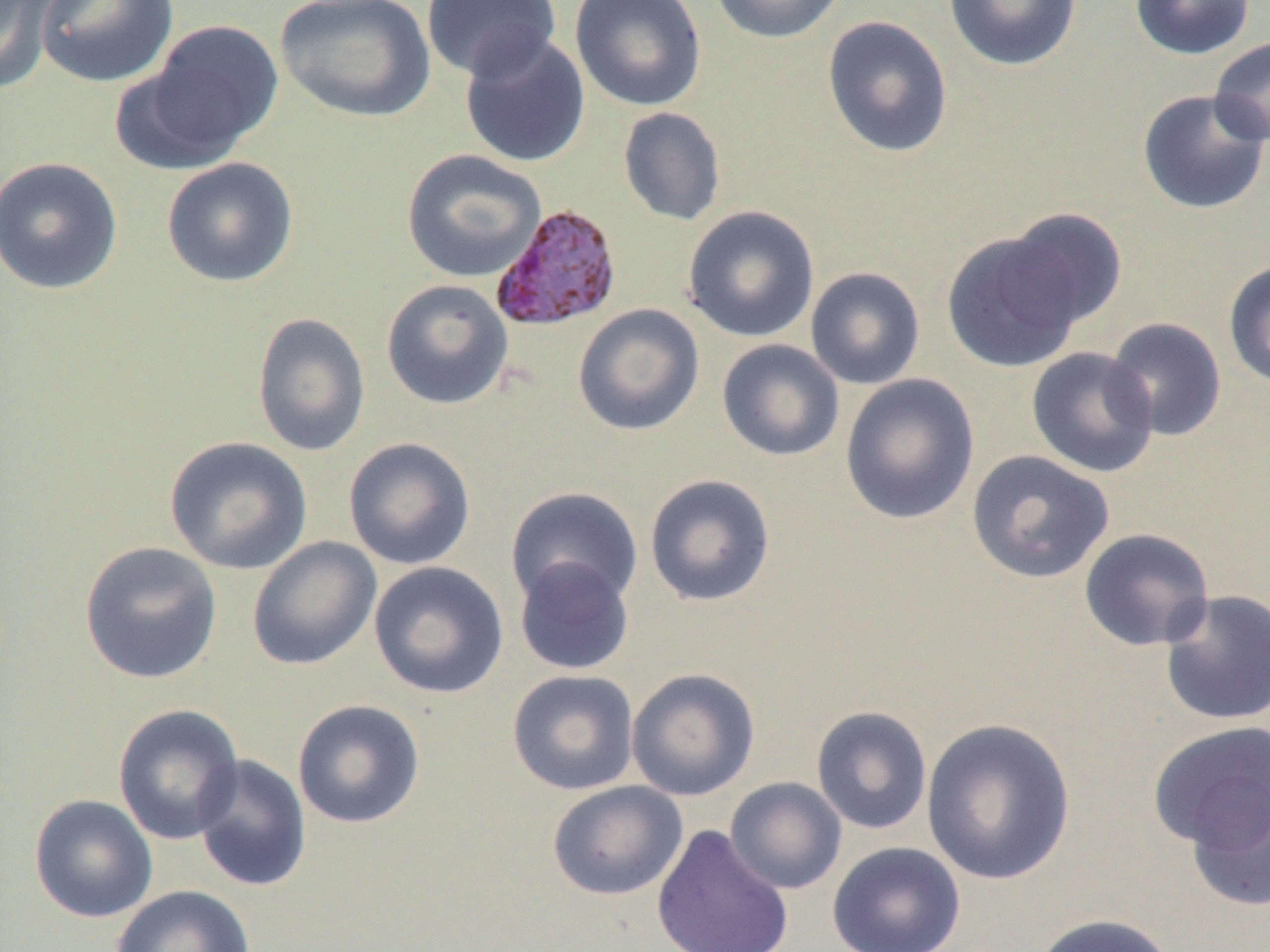

slide_level_diagnosis: Plasmodium vivax
field_of_view: one of a larger specimen
image_size: 1270×952 pixels
plasmodium_vivax_infected_red_blood_cell_locations: 'approximate bounding boxes as (x1, y1, x2, y2) in pixels: (490, 203, 622, 331)'
preparation: thin blood smear
magnification: 1000x
modality: light microscopy
uninfected_red_blood_cell_locations: 'approximate bounding boxes as (x1, y1, x2, y2) in pixels: (1, 0, 60, 94), (36, 0, 178, 88), (275, 0, 436, 123), (421, 0, 561, 82), (570, 0, 707, 112), (710, 0, 846, 44), (943, 0, 1083, 72), (1130, 0, 1255, 60), (821, 15, 954, 158), (140, 20, 284, 161), (459, 32, 591, 168), (1209, 36, 1270, 147), (1136, 89, 1270, 215), (618, 107, 726, 226), (401, 149, 547, 283), (0, 156, 123, 295), (161, 157, 298, 287), (682, 205, 820, 343), (1003, 208, 1128, 329), (941, 230, 1086, 373), (1223, 260, 1270, 389), (805, 266, 926, 390), (381, 279, 514, 410), (573, 303, 705, 436), (252, 311, 371, 457), (1104, 317, 1227, 441), (716, 338, 845, 461), (1026, 346, 1160, 479), (839, 373, 979, 525), (164, 436, 313, 575), (342, 436, 476, 570), (966, 449, 1115, 584), (644, 474, 776, 607), (505, 486, 644, 611), (1079, 527, 1215, 652), (247, 536, 382, 670), (79, 541, 223, 685), (514, 557, 635, 676), (368, 561, 509, 699), (1159, 588, 1270, 726), (626, 667, 761, 801), (507, 669, 640, 795), (292, 699, 426, 829), (112, 704, 245, 844), (811, 705, 932, 835), (920, 717, 1076, 886), (1148, 721, 1270, 856), (191, 753, 312, 892), (1185, 775, 1270, 913), (725, 777, 847, 894), (547, 780, 688, 900), (28, 793, 158, 923), (651, 824, 794, 952), (827, 841, 966, 952), (111, 884, 256, 952), (1030, 913, 1177, 952)'